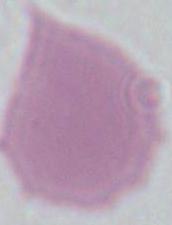

modality = micrograph
identification = red blood cell
magnification = 1000x